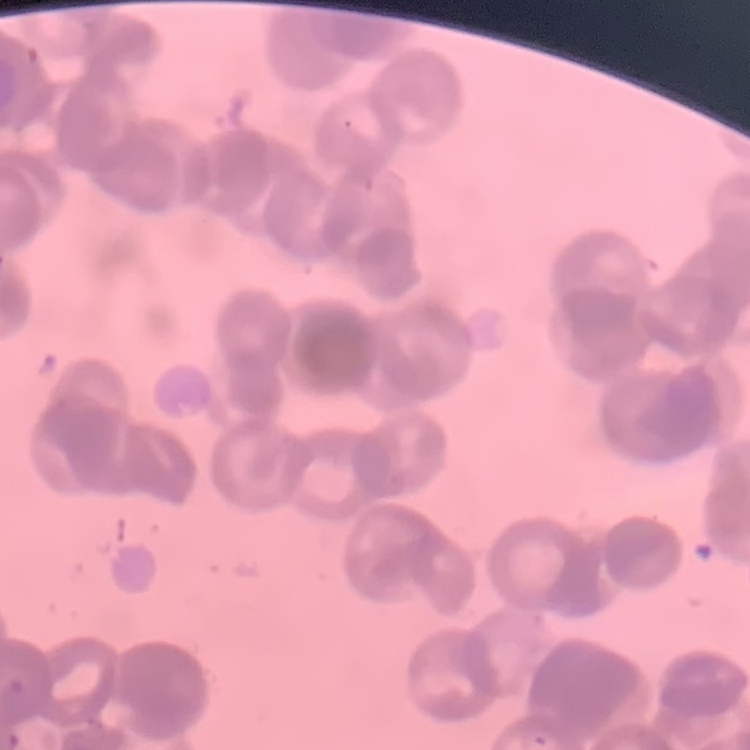
Summary:
  - Erythrocyte morphology: rouleaux formation
  - Preparation: thin blood film
  - Image type: one tile cut from a larger photomicrograph
  - Stain: Field's or Giemsa